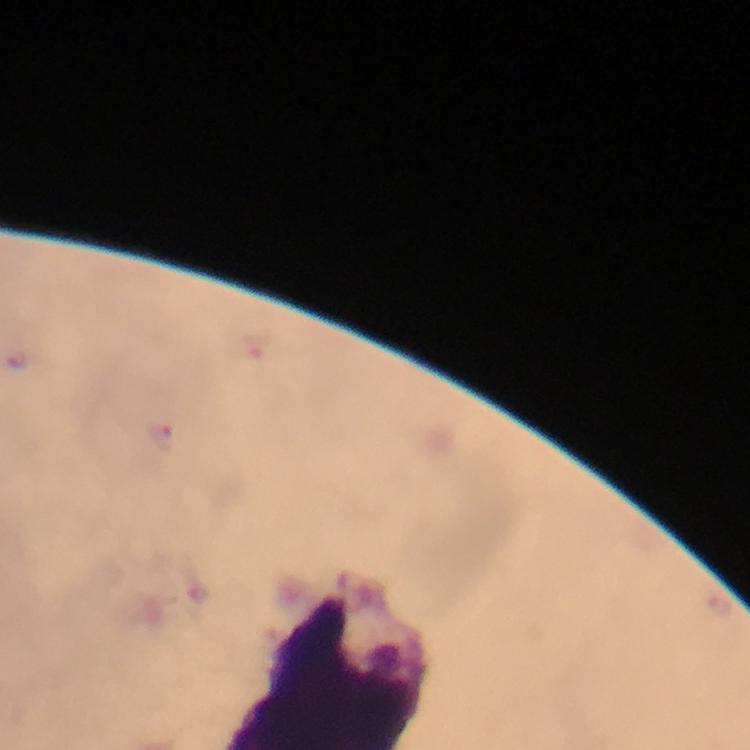

stain = Giemsa
cropped from = a single field of view
preparation = thick blood film
immersion oil = used
magnification = 100x
Plasmodium parasite locations = approximate object centers, in pixels from the top-left corner: (x=161, y=438)
context = from a diagnostic examination for malaria
capture = smartphone camera through the microscope
image size = 750×750 pixels